Comment on the morphology of the red blood cells.
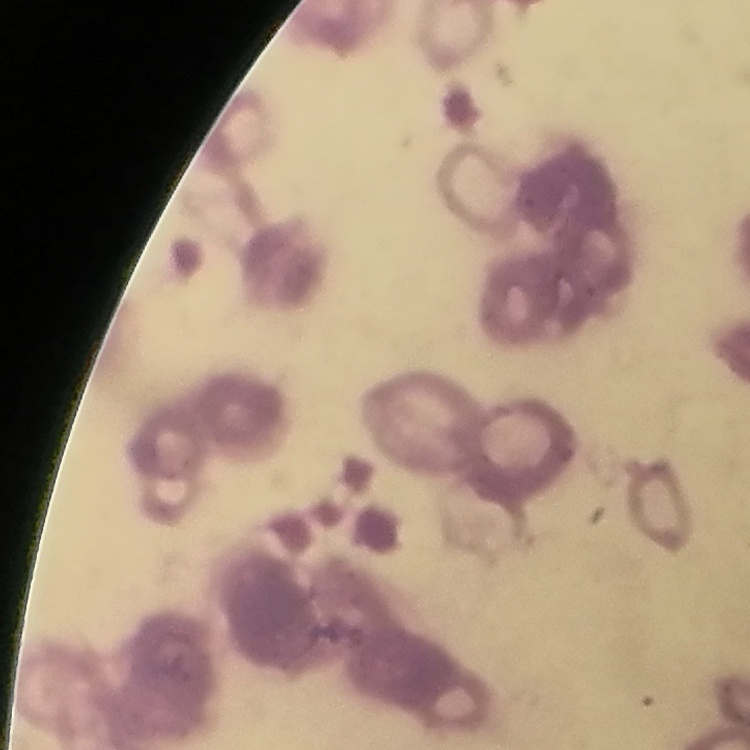
They show rouleaux formation.

Summary:
  - Image type: square crop of a larger photomicrograph
  - Stain: Field's or Giemsa
  - Preparation: thin blood smear